Comment on the morphology of the erythrocytes.
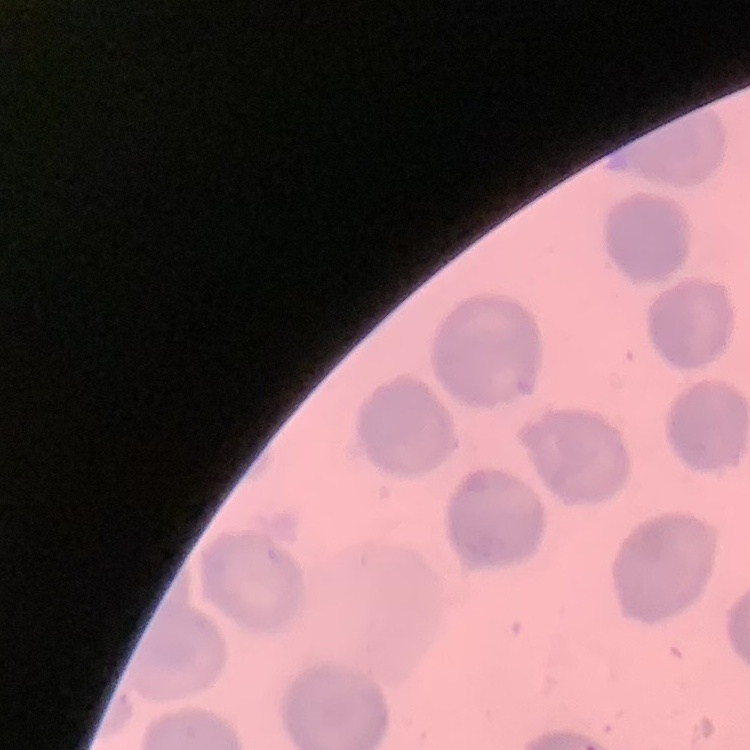

They show no rouleaux formation.

stain = Field's or Giemsa
preparation = thin blood film
image type = one tile cut from a larger photomicrograph